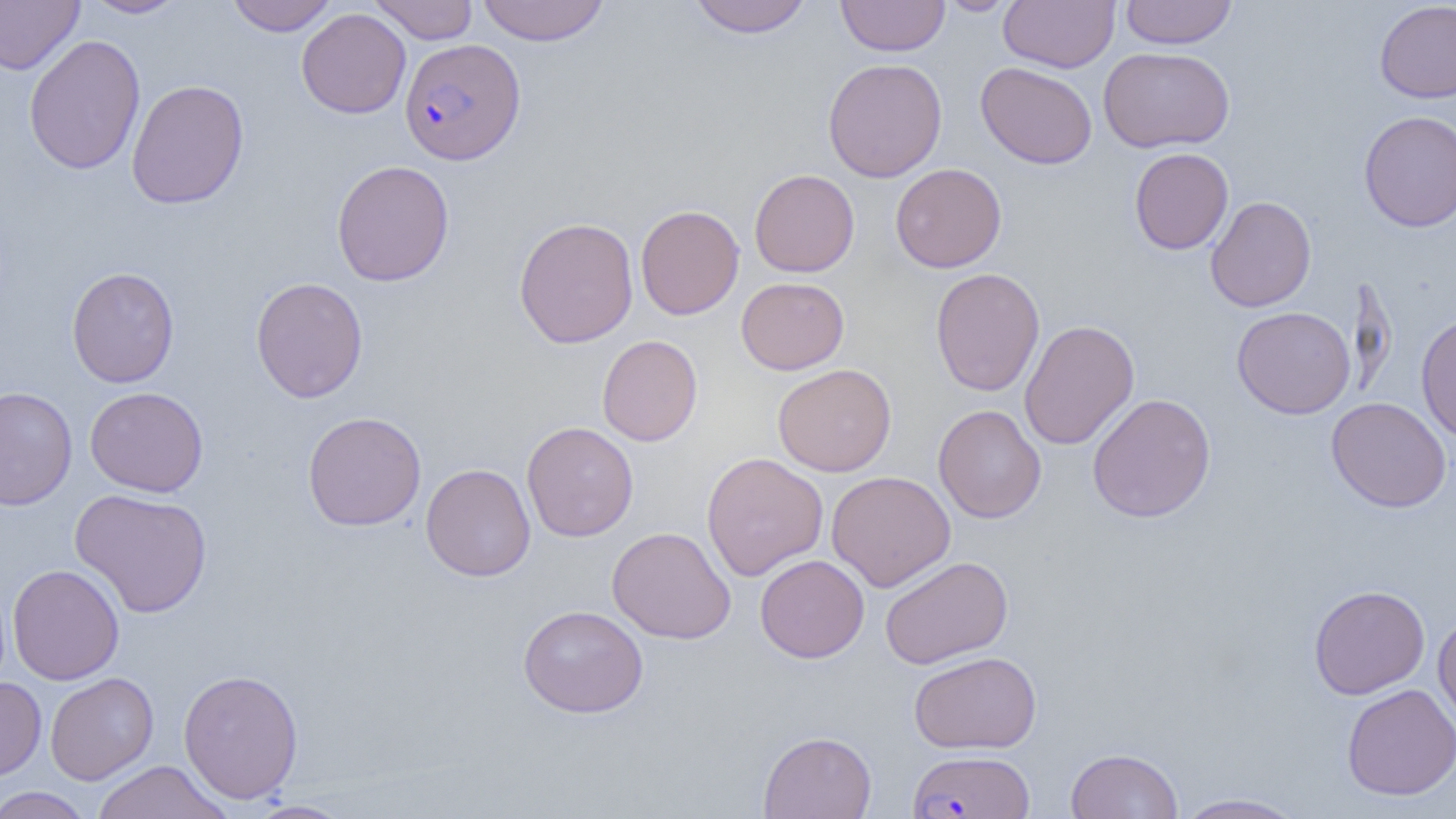
Approximate bounding boxes as (x1, y1, x2, y2) in pixels. Plasmodium falciparum-infected red blood cell locations: (399, 38, 526, 165), (907, 749, 1034, 818). Uninfected red blood cell locations: (0, 0, 84, 75), (80, 0, 190, 18), (226, 0, 338, 36), (368, 0, 479, 44), (476, 0, 611, 46), (687, 0, 814, 38), (836, 0, 949, 56), (937, 0, 1021, 15), (999, 0, 1120, 73), (1119, 0, 1237, 49), (1374, 1, 1456, 104), (297, 8, 411, 119), (23, 34, 145, 175), (1098, 46, 1235, 153), (822, 58, 947, 182), (975, 62, 1098, 169), (126, 79, 249, 209), (1359, 110, 1456, 231), (1129, 148, 1234, 254), (331, 160, 455, 286), (890, 163, 1007, 273), (749, 169, 860, 277), (1205, 196, 1317, 312), (635, 204, 744, 320), (513, 216, 639, 348), (66, 267, 179, 388), (930, 267, 1045, 396), (250, 277, 368, 403), (736, 277, 849, 374), (1231, 306, 1356, 419), (1415, 313, 1456, 442), (1018, 319, 1139, 450), (597, 335, 703, 446), (772, 363, 896, 477), (0, 386, 77, 510), (85, 386, 209, 498), (1086, 393, 1216, 523), (1326, 397, 1451, 513), (933, 404, 1046, 523), (302, 411, 426, 532), (522, 421, 639, 542), (701, 452, 828, 581), (420, 463, 535, 582), (826, 470, 956, 592), (70, 488, 213, 618), (607, 526, 736, 644), (755, 554, 869, 663), (880, 556, 1013, 669), (7, 564, 125, 685), (1308, 584, 1430, 699), (517, 604, 649, 718), (1433, 614, 1456, 731), (908, 651, 1042, 754), (178, 668, 304, 804), (45, 672, 159, 785), (0, 677, 47, 781), (1341, 683, 1456, 800), (758, 730, 877, 819), (1065, 748, 1184, 818), (90, 760, 233, 819), (0, 786, 94, 819), (1173, 792, 1309, 819), (246, 800, 355, 819). Slide-level diagnosis: Plasmodium falciparum. Image is 1456×819 pixels. Single field of view. Light microscopy. Captured at 1000x magnification. Thin blood smear.